Classify this cell by malaria status.
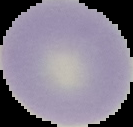

It is uninfected.

From a thin blood film. The area outside the segmented cell region is set to black. Image is 133×127 pixels.